Locate every blood parasite and identify its species.
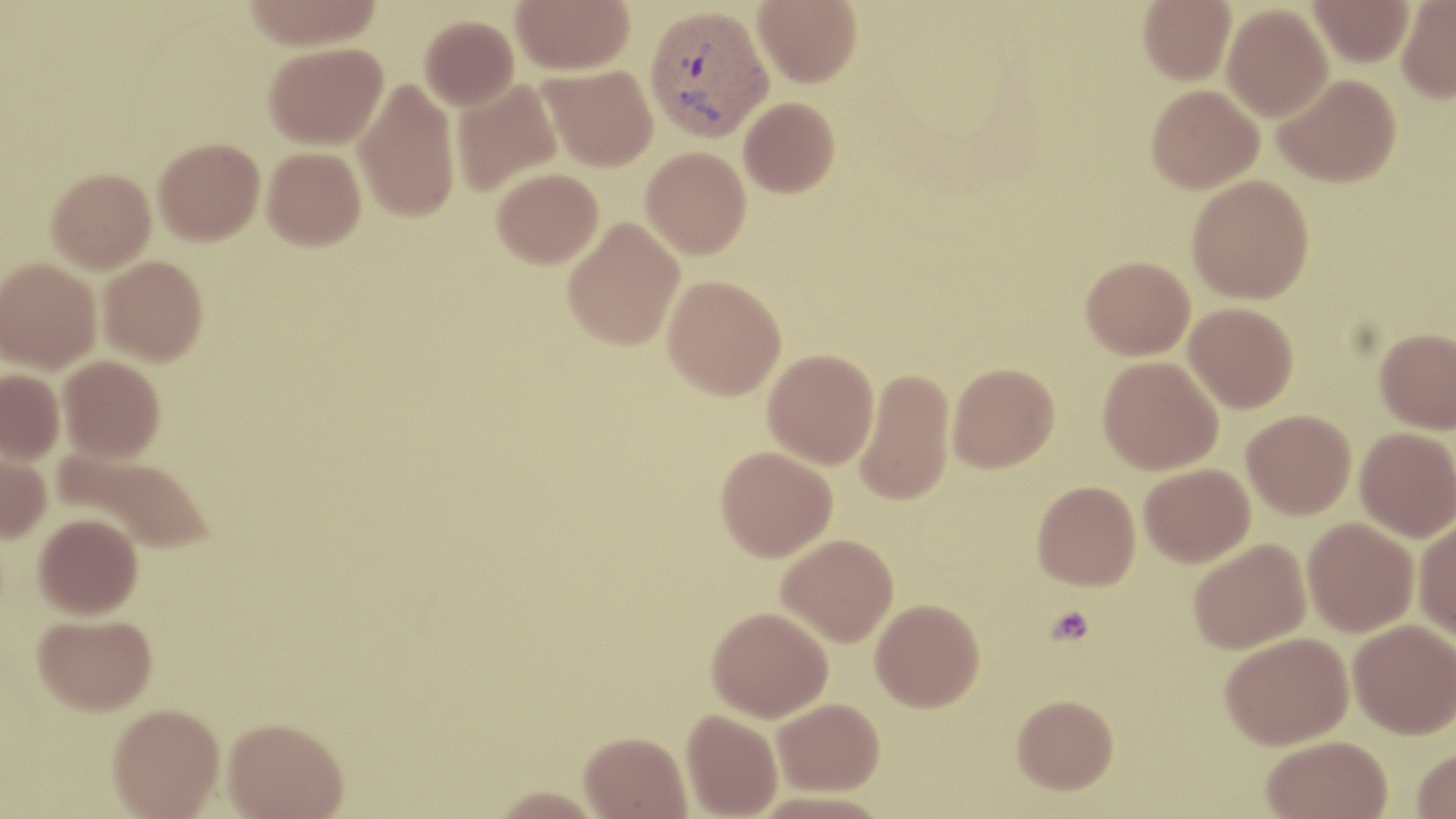
Approximate bounding boxes as (x1,y1)-(x2,y2) corner pairs in pixels.
Plasmodium vivax-infected red blood cells: (644,4)-(773,142).
No Plasmodium falciparum, Plasmodium ovale, Plasmodium malariae, Babesia divergens, or Trypanosoma brucei observed.

slide-level diagnosis = Plasmodium vivax
uninfected red blood cell locations = approximate bounding boxes as (x1,y1)-(x2,y2) corner pairs in pixels: (244,0)-(383,50), (511,0)-(634,74), (752,0)-(862,87), (1138,0)-(1236,85), (1308,0)-(1414,67), (1396,0)-(1456,101), (1222,4)-(1333,121), (420,15)-(519,110), (263,42)-(387,149), (539,65)-(658,171), (1273,73)-(1401,187), (353,77)-(460,223), (451,79)-(562,196), (1146,84)-(1264,193), (738,97)-(840,197), (153,137)-(264,245), (262,146)-(366,250), (641,146)-(751,259), (47,167)-(156,271), (492,168)-(603,268), (1187,175)-(1314,303), (562,217)-(685,351), (98,255)-(208,365), (1081,255)-(1195,360), (0,258)-(101,372), (662,275)-(786,400), (1184,302)-(1299,413), (1374,327)-(1456,433), (763,349)-(879,469), (59,355)-(165,462), (1098,356)-(1223,475), (948,361)-(1059,472), (854,367)-(956,506), (0,369)-(64,463), (1242,410)-(1356,519), (1355,427)-(1455,542), (0,443)-(51,544), (715,446)-(837,561), (53,449)-(215,554), (1139,463)-(1255,567), (1032,480)-(1141,590), (34,513)-(143,619), (1413,516)-(1456,640), (1303,518)-(1419,636), (776,533)-(898,646), (1188,538)-(1311,653), (870,598)-(985,711), (707,606)-(833,721), (32,613)-(157,715), (1348,619)-(1456,739), (1220,632)-(1353,749), (1012,694)-(1119,794), (773,697)-(884,795), (107,704)-(224,818), (681,709)-(782,818), (222,718)-(348,819), (579,731)-(692,818), (1261,735)-(1393,819), (1411,748)-(1456,819), (489,786)-(605,818)
field of view = one of a larger specimen
preparation = thin blood film
magnification = 1000x
platelet locations = approximate bounding boxes as (x1,y1)-(x2,y2) corner pairs in pixels: (1047,606)-(1095,645)
stain = May-Grünwald-Giemsa
image size = 1456×819 pixels
modality = optical microscopy